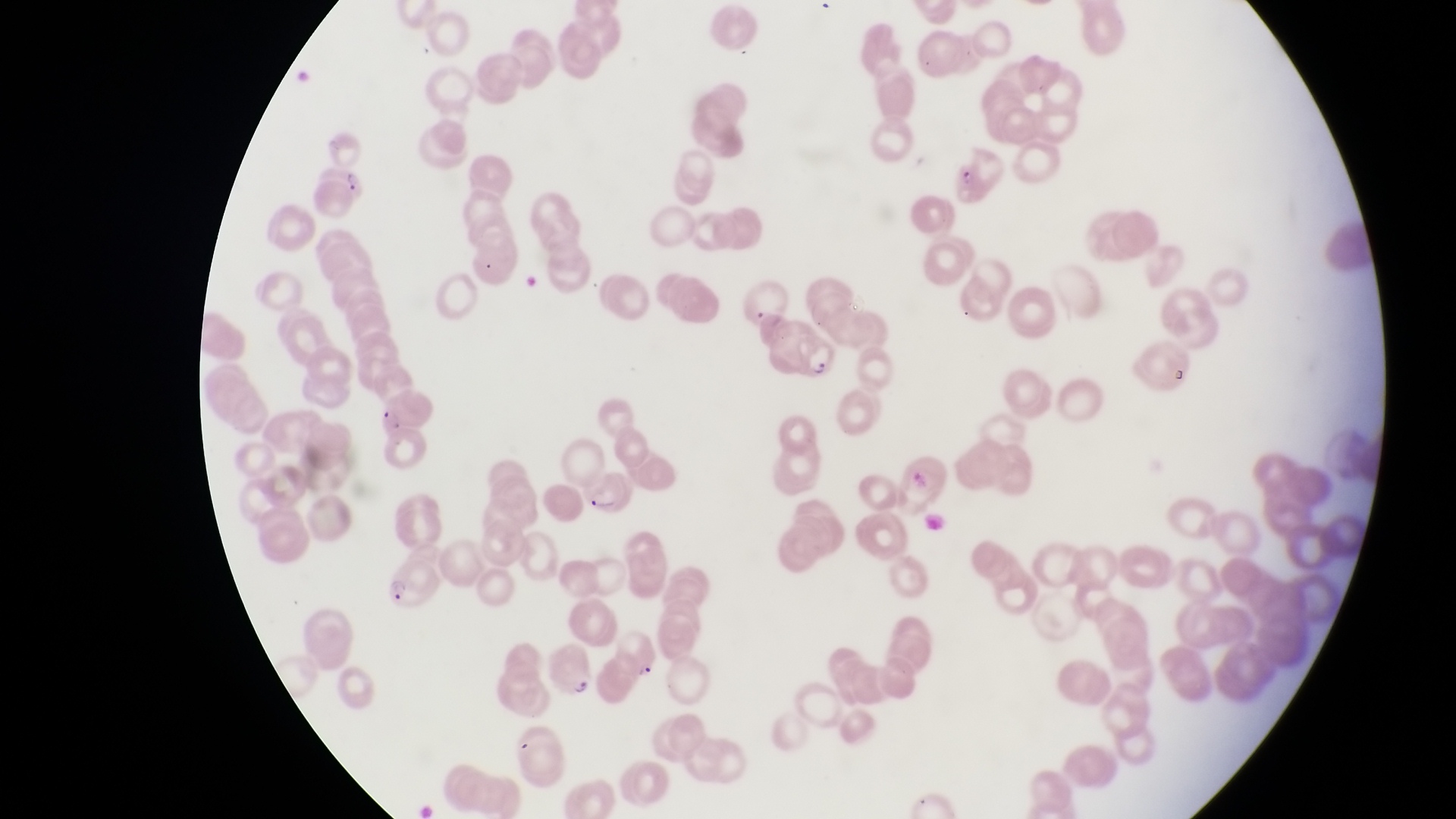
country: Uganda
preparation: thin blood film
parasitised_red_blood_cell_locations: 'approximate bounding boxes as (left, top, right, bottom) in pixels: (949, 143, 1009, 215), (307, 162, 370, 218), (785, 331, 843, 387), (581, 470, 634, 515), (377, 549, 441, 612), (545, 640, 600, 703)'
capture: smartphone photograph through the eyepiece of an Olympus CX-23 microscope
image_size: 1456×819 pixels
field_of_view: single
magnification: 1000x